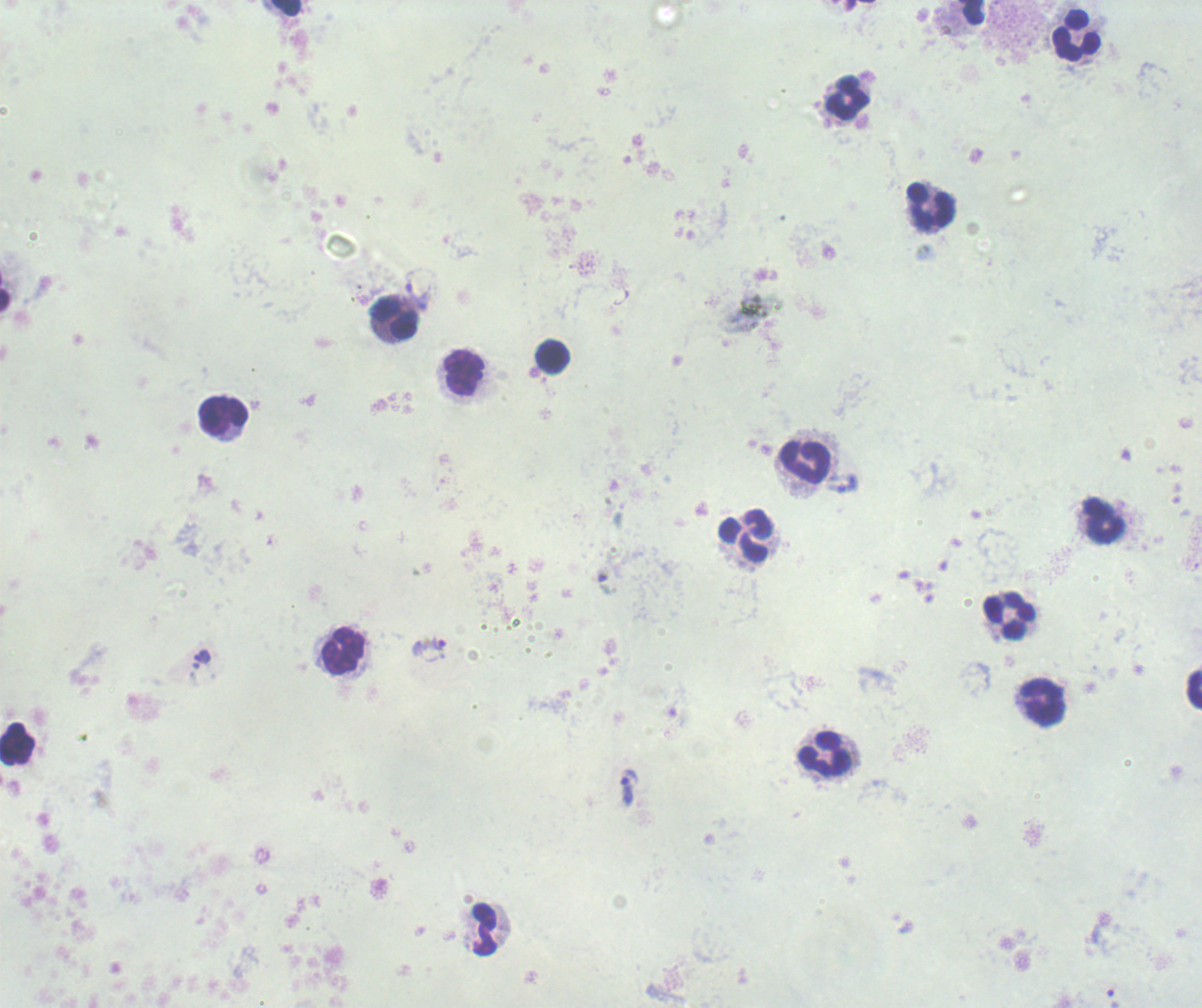
coordinate format = approximate centers as {x, y} in pixels
leukocyte locations = {972, 12}, {1077, 37}, {849, 98}, {929, 206}, {395, 320}, {553, 356}, {464, 372}, {224, 416}, {805, 463}, {1102, 521}, {746, 535}, {1008, 617}, {344, 652}, {1195, 691}, {1042, 702}, {17, 743}, {827, 754}, {485, 929}
trophozoite locations = {434, 644}, {203, 656}, {629, 787}, {1112, 998}
image size = 1202×1008 pixels
result = Plasmodium parasites identified
field of view = single
preparation = thick smear of blood
stain = Romanowsky
context = previously used in an actual diagnosis
background quality = unsatisfactory
magnification = 100x